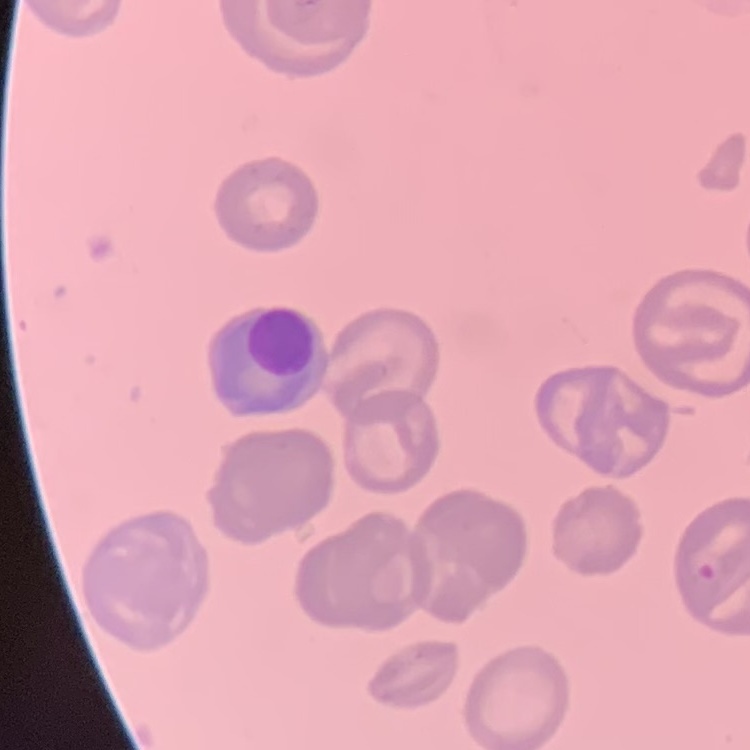
The erythrocytes exhibit no rouleaux formation. Square crop of a larger photomicrograph. Stained with either Field's or Giemsa. Thin blood film.